Assess this cell for malaria.
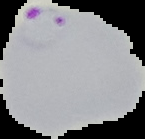

It is parasitized.

Summary:
  - Preparation: thin blood smear
  - Image size: 145×139 pixels
  - Image type: cell region segmented out of the field of view; surrounding area masked to black